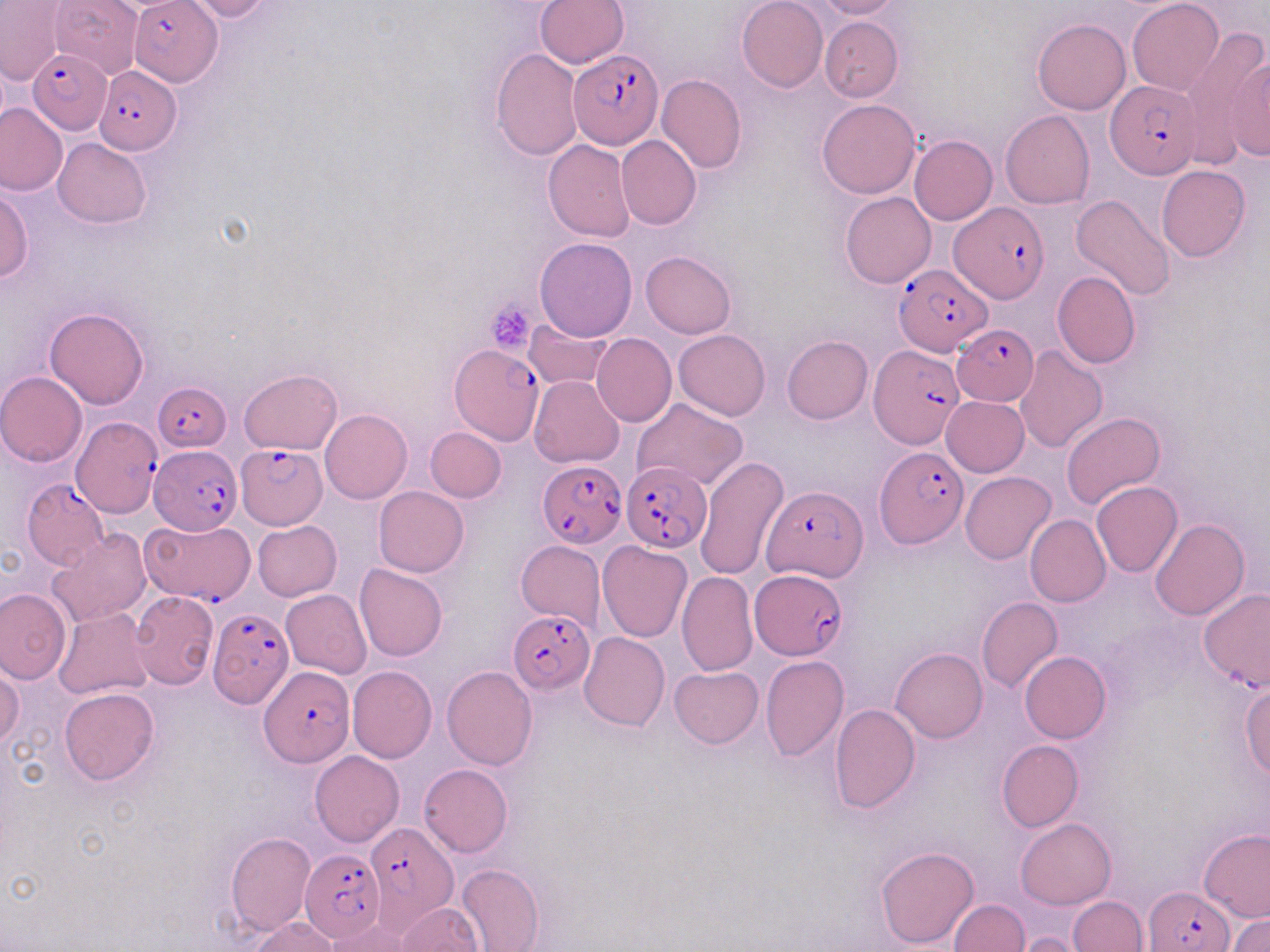

Summary:
  - Coordinate format: approximate bounding boxes as named x1/y1/x2/y2 corners in pixels
  - Uninfected red blood cell locations: (x1=47, y1=0, x2=144, y2=80), (x1=533, y1=0, x2=629, y2=67), (x1=737, y1=0, x2=828, y2=91), (x1=813, y1=0, x2=904, y2=20), (x1=1127, y1=0, x2=1224, y2=95), (x1=1, y1=1, x2=66, y2=87), (x1=180, y1=1, x2=278, y2=22), (x1=819, y1=17, x2=902, y2=102), (x1=1033, y1=18, x2=1131, y2=115), (x1=1181, y1=27, x2=1268, y2=162), (x1=490, y1=48, x2=582, y2=160), (x1=1226, y1=49, x2=1270, y2=161), (x1=657, y1=74, x2=746, y2=173), (x1=817, y1=100, x2=919, y2=199), (x1=0, y1=103, x2=66, y2=196), (x1=1000, y1=110, x2=1095, y2=209), (x1=615, y1=134, x2=702, y2=230), (x1=910, y1=136, x2=997, y2=224), (x1=53, y1=138, x2=153, y2=228), (x1=543, y1=139, x2=634, y2=242), (x1=1157, y1=166, x2=1250, y2=262), (x1=0, y1=185, x2=32, y2=283), (x1=841, y1=192, x2=935, y2=288), (x1=1071, y1=195, x2=1174, y2=301), (x1=534, y1=236, x2=639, y2=342), (x1=640, y1=251, x2=736, y2=338), (x1=1052, y1=270, x2=1140, y2=368), (x1=44, y1=307, x2=149, y2=410), (x1=524, y1=319, x2=611, y2=389), (x1=674, y1=330, x2=770, y2=421), (x1=592, y1=333, x2=676, y2=426), (x1=782, y1=335, x2=873, y2=423), (x1=1014, y1=346, x2=1107, y2=453), (x1=239, y1=369, x2=343, y2=455), (x1=0, y1=371, x2=88, y2=466), (x1=529, y1=375, x2=625, y2=468), (x1=942, y1=396, x2=1030, y2=477), (x1=632, y1=398, x2=747, y2=491), (x1=321, y1=409, x2=413, y2=503), (x1=1061, y1=412, x2=1166, y2=509), (x1=425, y1=427, x2=506, y2=501), (x1=695, y1=456, x2=790, y2=580), (x1=961, y1=471, x2=1055, y2=564), (x1=1091, y1=481, x2=1183, y2=577), (x1=373, y1=487, x2=469, y2=576), (x1=1025, y1=515, x2=1110, y2=606), (x1=1150, y1=517, x2=1250, y2=620), (x1=253, y1=520, x2=342, y2=600), (x1=47, y1=529, x2=152, y2=629), (x1=515, y1=540, x2=605, y2=631), (x1=597, y1=542, x2=692, y2=642), (x1=354, y1=563, x2=449, y2=661), (x1=676, y1=572, x2=759, y2=675), (x1=280, y1=588, x2=372, y2=678), (x1=0, y1=589, x2=70, y2=684), (x1=1198, y1=589, x2=1269, y2=691), (x1=129, y1=591, x2=219, y2=688), (x1=976, y1=597, x2=1063, y2=695), (x1=53, y1=608, x2=154, y2=701), (x1=578, y1=631, x2=669, y2=731), (x1=891, y1=647, x2=987, y2=742), (x1=1019, y1=652, x2=1111, y2=743), (x1=760, y1=655, x2=850, y2=761), (x1=0, y1=665, x2=23, y2=750), (x1=348, y1=666, x2=436, y2=763), (x1=441, y1=666, x2=537, y2=770), (x1=669, y1=666, x2=763, y2=748), (x1=1240, y1=683, x2=1270, y2=777), (x1=59, y1=687, x2=160, y2=785), (x1=830, y1=705, x2=920, y2=813), (x1=996, y1=740, x2=1084, y2=831), (x1=310, y1=751, x2=404, y2=847), (x1=418, y1=763, x2=512, y2=858), (x1=1016, y1=818, x2=1117, y2=909), (x1=1199, y1=830, x2=1270, y2=923), (x1=226, y1=833, x2=317, y2=936), (x1=875, y1=845, x2=980, y2=950), (x1=457, y1=863, x2=544, y2=952), (x1=1067, y1=896, x2=1148, y2=951), (x1=947, y1=899, x2=1029, y2=951), (x1=397, y1=902, x2=483, y2=951), (x1=1230, y1=914, x2=1269, y2=952), (x1=250, y1=917, x2=341, y2=951), (x1=323, y1=917, x2=412, y2=951), (x1=1013, y1=932, x2=1092, y2=952)
  - Plasmodium falciparum-infected red blood cell locations: (x1=129, y1=4, x2=222, y2=88), (x1=28, y1=49, x2=111, y2=133), (x1=568, y1=49, x2=663, y2=147), (x1=92, y1=64, x2=182, y2=153), (x1=1107, y1=79, x2=1200, y2=178), (x1=946, y1=200, x2=1049, y2=306), (x1=892, y1=259, x2=989, y2=355), (x1=951, y1=326, x2=1039, y2=405), (x1=868, y1=341, x2=965, y2=449), (x1=452, y1=344, x2=545, y2=444), (x1=154, y1=380, x2=233, y2=452), (x1=69, y1=415, x2=161, y2=516), (x1=149, y1=445, x2=243, y2=534), (x1=235, y1=445, x2=326, y2=528), (x1=876, y1=446, x2=969, y2=548), (x1=535, y1=456, x2=625, y2=545), (x1=624, y1=462, x2=712, y2=551), (x1=21, y1=478, x2=108, y2=569), (x1=763, y1=486, x2=866, y2=582), (x1=147, y1=521, x2=262, y2=621), (x1=750, y1=569, x2=848, y2=659), (x1=206, y1=604, x2=292, y2=709), (x1=508, y1=610, x2=596, y2=691), (x1=261, y1=666, x2=352, y2=766), (x1=363, y1=822, x2=459, y2=928), (x1=300, y1=851, x2=385, y2=940), (x1=1145, y1=886, x2=1233, y2=952)
  - Platelet locations: (x1=486, y1=298, x2=538, y2=356)
  - Slide-level diagnosis: Plasmodium falciparum
  - Stain: May-Grünwald-Giemsa
  - Field of view: one of a larger specimen
  - Preparation: thin blood smear
  - Modality: optical microscopy
  - Image size: 1270×952 pixels
  - Magnification: 1000x